Classify the preparation.
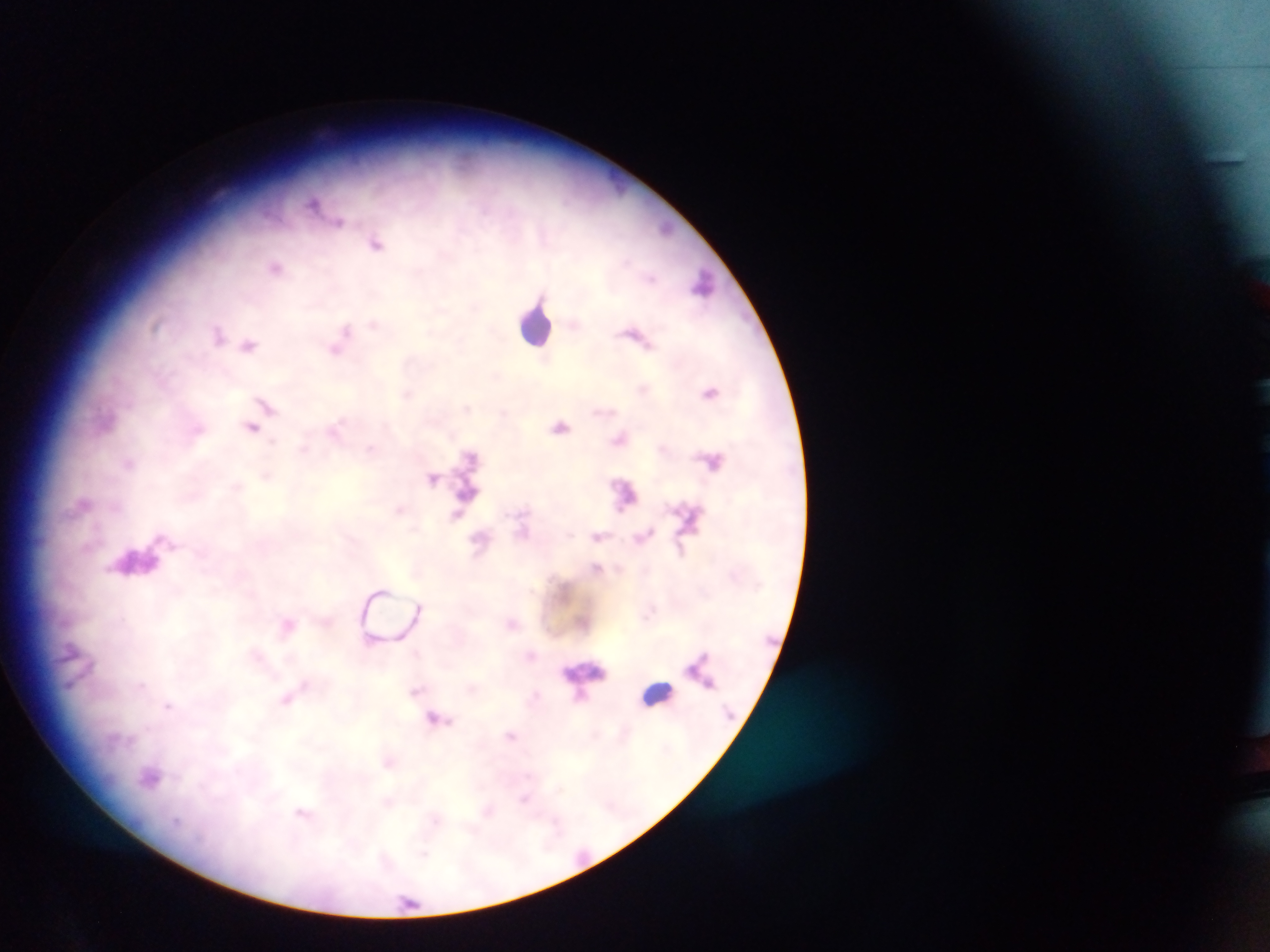

Thick blood smear.

Approximate centers as [x, y] in pixels.
Summary:
  - Plasmodium parasite locations: [314, 202], [339, 222], [375, 244], [276, 267], [703, 284], [373, 323], [344, 331], [218, 334], [249, 344], [336, 348], [710, 392], [407, 394], [266, 405], [252, 427], [561, 427], [335, 429], [198, 430], [619, 439], [304, 447], [371, 449], [128, 463], [433, 478], [399, 509], [457, 513], [599, 537], [481, 540], [596, 568], [419, 606], [287, 625], [141, 686], [416, 691], [288, 700], [168, 705], [437, 718], [510, 736], [388, 763], [151, 778], [524, 799], [303, 812]
  - Leukocyte locations: [536, 323], [138, 560], [585, 671], [656, 694]
  - Field of view: single
  - Capture: mobile-phone photograph through a microscope
  - Image size: 1270×952 pixels
  - Country: Ghana